Comment on the morphology of the red blood cells.
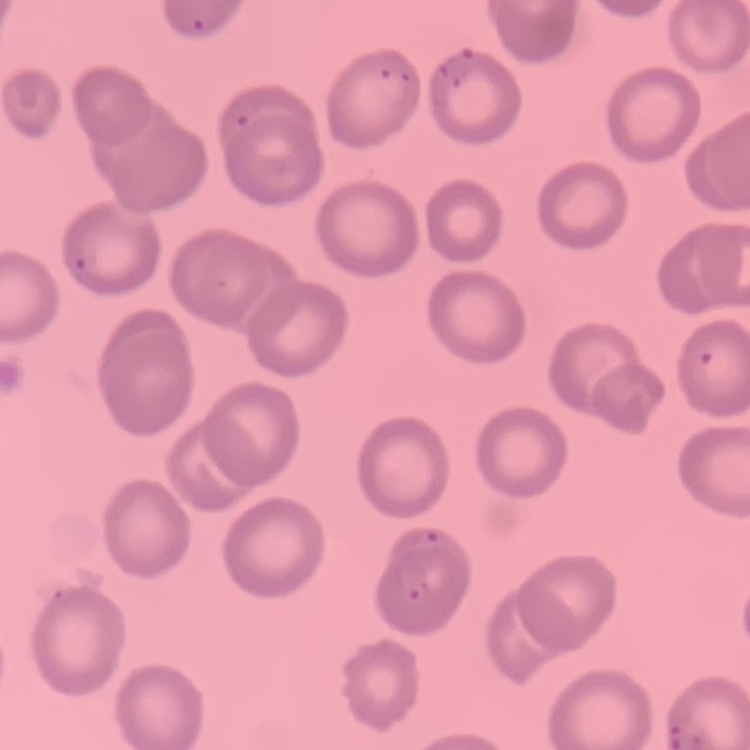

No rouleaux formation.

Thin blood smear. Field's or Giemsa stain. Square crop of a larger photomicrograph.